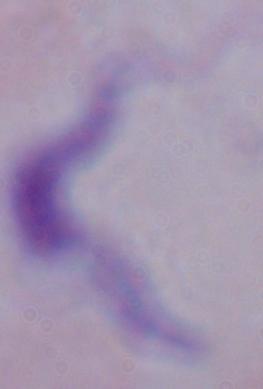
{
  "magnification": "1000x",
  "identification": "trypanosome",
  "modality": "photomicrograph"
}